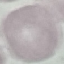
Result: no malaria parasites detected. Giemsa-stained preparation. Cell patch, automatically extracted from a larger field of view and resized to 64 × 64 pixels. Thin blood film. Acquired by smartphone through the microscope eyepiece.